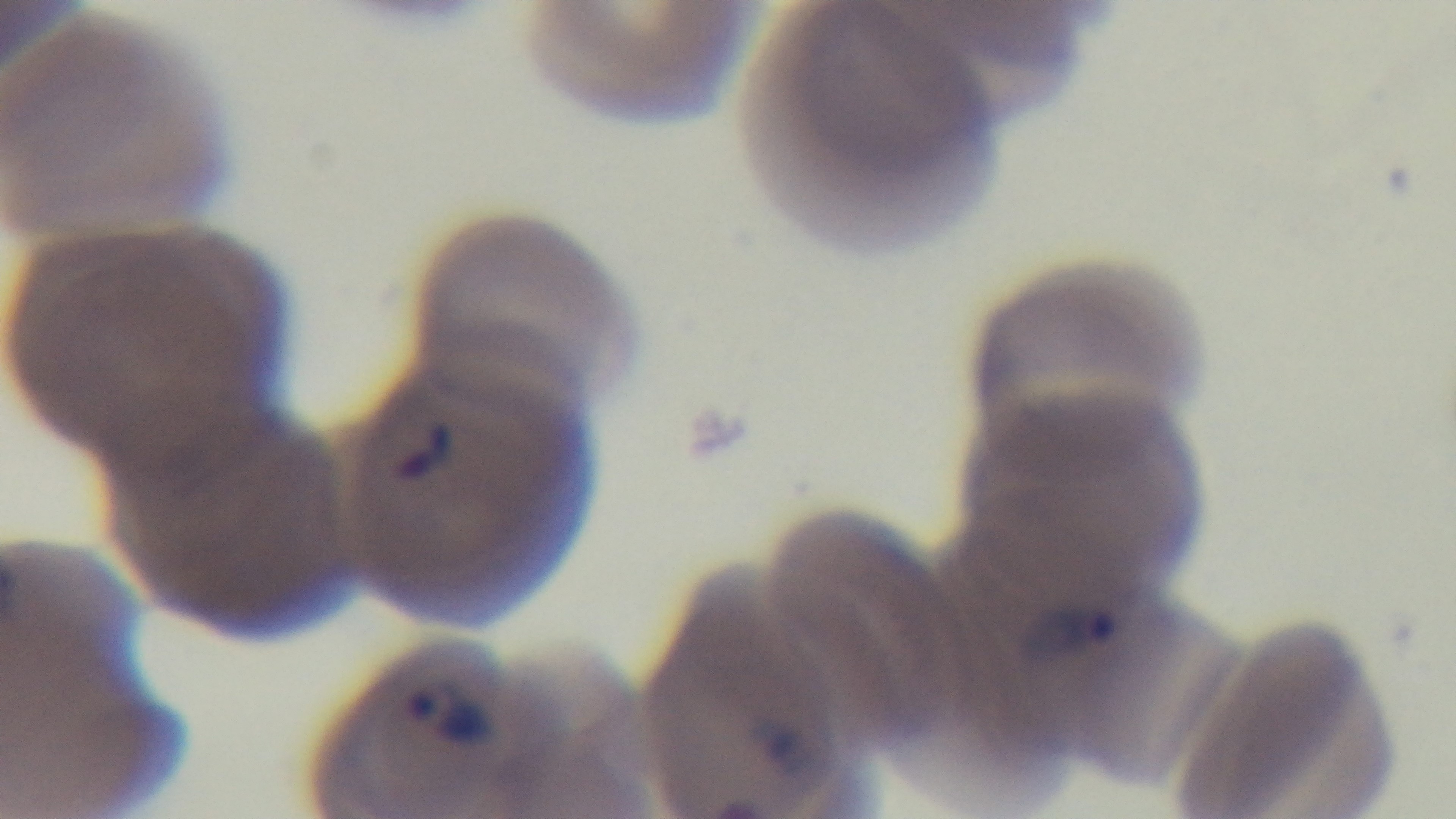 Giemsa stain. Mounted 4K digital camera. Single field of view. Malaria status: positive. Oil-immersion objective, 100x. Photomicrograph. Preparation: thin blood film.